Outline each Trypanosoma brucei.
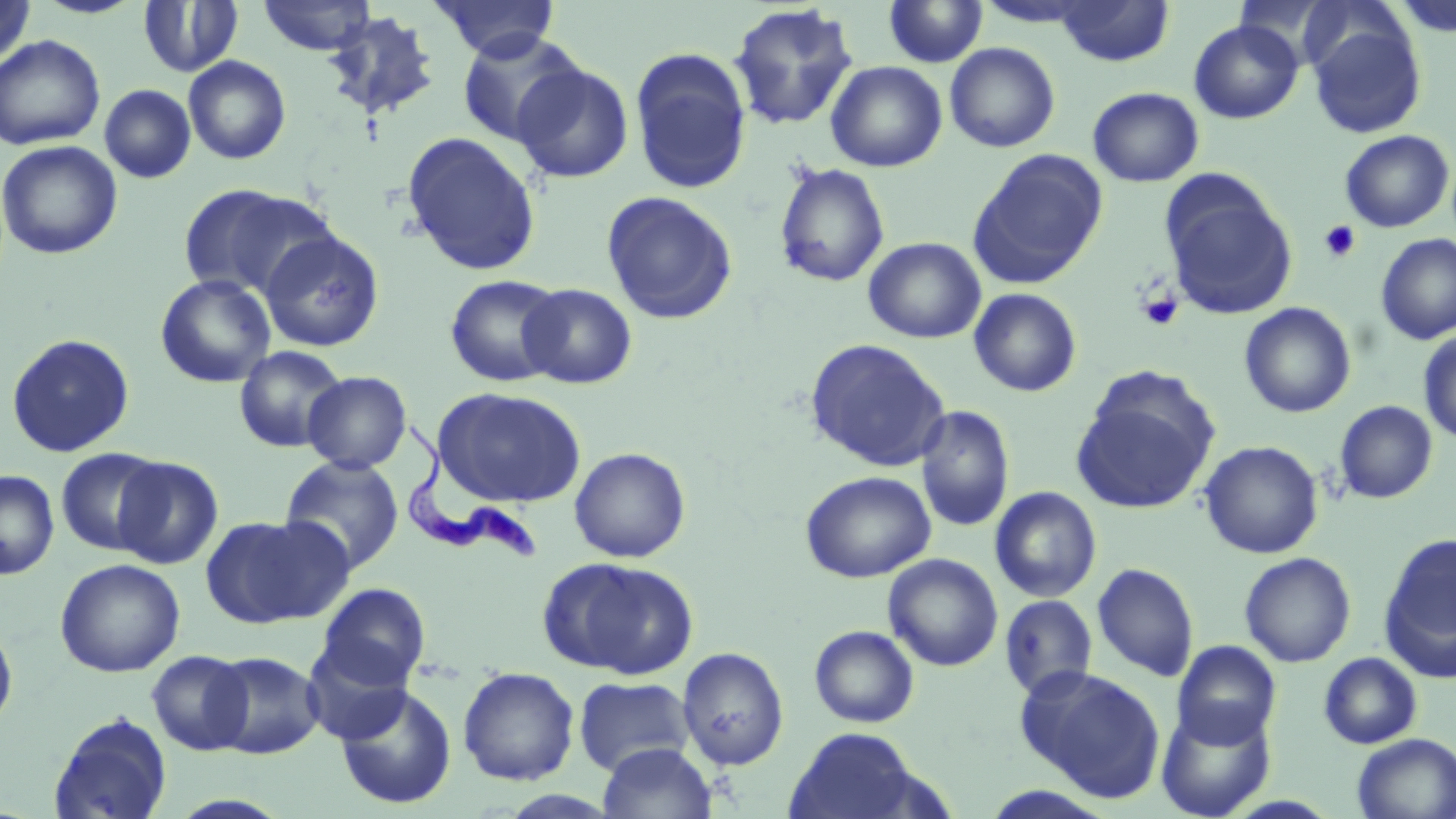
Approximate bounding boxes as [x1, y1, x2, y2] in pixels.
Trypanosoma brucei: [399, 418, 540, 561].

slide-level diagnosis = Trypanosoma brucei
modality = light microscopy
magnification = 1000x
preparation = thin blood film
image size = 1456×819 pixels
stain = May-Grünwald-Giemsa
platelet locations = approximate bounding boxes as [x1, y1, x2, y2] in pixels: [1318, 220, 1362, 263], [1136, 291, 1184, 331]
field of view = one of a larger specimen
uninfected red blood cell locations = approximate bounding boxes as [x1, y1, x2, y2] in pixels: [0, 0, 36, 69], [30, 0, 147, 19], [258, 0, 377, 56], [430, 0, 560, 62], [1054, 0, 1174, 67], [1297, 0, 1413, 84], [1393, 0, 1456, 39], [138, 1, 243, 77], [882, 1, 987, 68], [726, 2, 859, 131], [322, 11, 441, 123], [1306, 17, 1426, 138], [1188, 19, 1303, 124], [455, 31, 587, 148], [0, 35, 105, 150], [945, 42, 1060, 152], [630, 47, 753, 195], [183, 55, 291, 164], [511, 61, 634, 183], [826, 61, 947, 172], [99, 84, 196, 183], [1087, 87, 1204, 187], [1339, 130, 1454, 232], [401, 131, 542, 276], [0, 139, 123, 260], [969, 150, 1108, 288], [773, 162, 890, 287], [1160, 175, 1298, 320], [177, 183, 329, 300], [601, 190, 739, 325], [259, 230, 385, 353], [1374, 233, 1456, 345], [863, 237, 986, 343], [155, 274, 277, 388], [444, 274, 566, 388], [518, 283, 637, 389], [968, 288, 1082, 397], [1239, 302, 1356, 418], [1418, 330, 1456, 444], [5, 333, 135, 457], [804, 338, 951, 471], [233, 345, 348, 453], [302, 371, 412, 473], [1071, 372, 1219, 515], [433, 387, 586, 507], [1335, 400, 1437, 503], [915, 405, 1014, 532], [1199, 440, 1323, 558], [569, 447, 691, 563], [56, 448, 168, 555], [112, 456, 223, 569], [279, 456, 404, 574], [0, 470, 59, 579], [800, 470, 936, 583], [989, 486, 1101, 602], [201, 514, 348, 629], [1379, 534, 1456, 681], [1239, 552, 1356, 667], [883, 553, 1003, 671], [543, 557, 698, 679], [54, 558, 185, 678], [1092, 562, 1199, 682], [317, 583, 431, 688], [999, 594, 1097, 701], [0, 620, 18, 734], [809, 625, 919, 728], [301, 639, 414, 745], [1172, 640, 1281, 748], [677, 646, 789, 770], [146, 650, 253, 754], [207, 651, 324, 759], [1318, 652, 1422, 749], [1016, 665, 1166, 801], [458, 666, 580, 785], [573, 676, 696, 777], [334, 685, 457, 809], [1156, 703, 1276, 818], [48, 712, 173, 818], [783, 727, 928, 819], [1352, 733, 1456, 819], [597, 742, 718, 819], [164, 794, 296, 818]